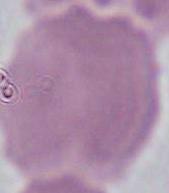
Captured at 1000x magnification. Micrograph. A red blood cell is seen.